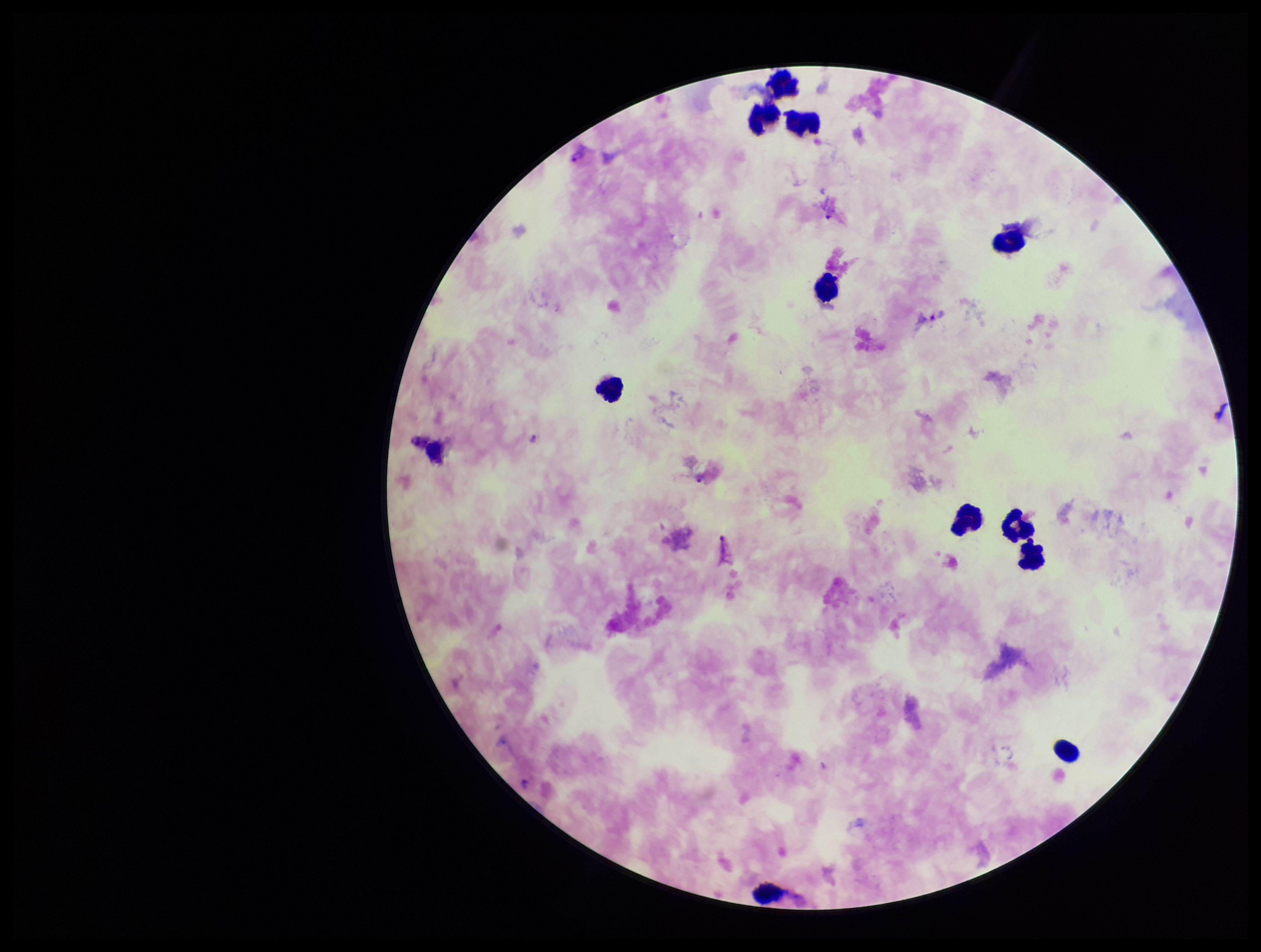

Summary:
  - Field of view: one from this slide
  - Preparation: thick smear
  - Species reported for this patient: Plasmodium vivax
  - Capture: smartphone photograph through the microscope eyepiece
  - Stain: Giemsa
  - Plasmodium parasites: detected
  - Image size: 1261×952 pixels
  - Parasite count: 4
  - Leukocyte count: 12
  - Patient malaria status: positive